Outline each Plasmodium falciparum-infected red blood cell.
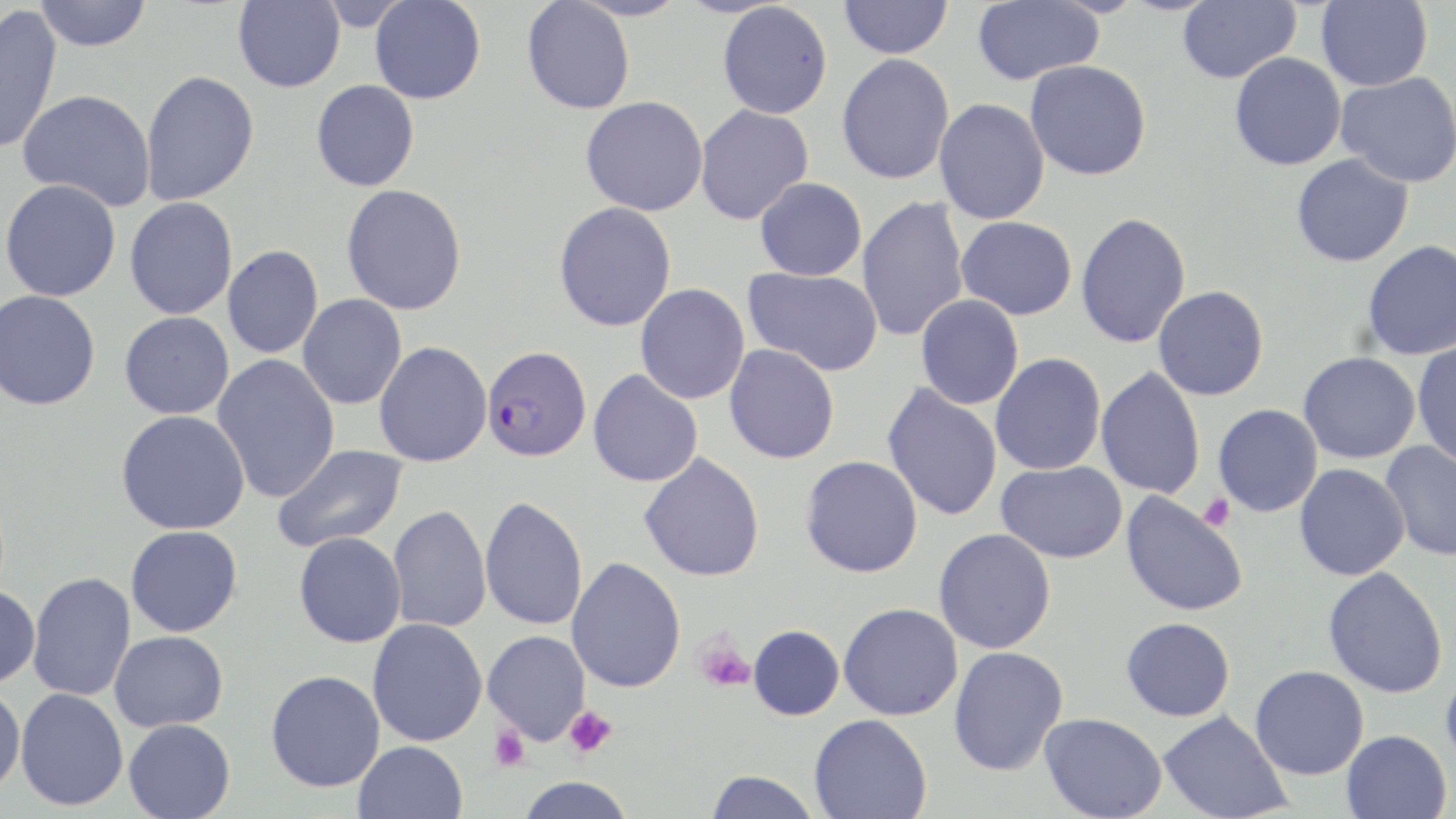
Approximate bounding boxes as (x1, y1, x2, y2) in pixels.
Plasmodium falciparum-infected red blood cells: (482, 345, 592, 462).

slide_level_diagnosis: Plasmodium falciparum
uninfected_red_blood_cell_locations: 'approximate bounding boxes as (x1, y1, x2, y2) in pixels: (34, 0, 152, 52), (233, 0, 345, 93), (370, 0, 485, 104), (838, 0, 953, 59), (971, 0, 1105, 85), (1177, 0, 1300, 83), (1316, 0, 1432, 91), (521, 1, 635, 114), (717, 2, 833, 119), (0, 3, 63, 156), (1229, 52, 1346, 170), (837, 53, 955, 185), (1025, 60, 1151, 181), (140, 70, 260, 206), (1336, 72, 1456, 188), (311, 80, 420, 192), (18, 89, 156, 212), (580, 96, 708, 216), (934, 98, 1050, 225), (695, 104, 814, 225), (1291, 153, 1414, 267), (755, 177, 867, 281), (1, 179, 121, 302), (341, 184, 467, 315), (125, 196, 238, 319), (856, 196, 969, 342), (553, 202, 677, 332), (1075, 212, 1191, 348), (956, 216, 1077, 320), (1362, 240, 1456, 360), (222, 245, 323, 359), (744, 267, 883, 376), (635, 284, 750, 404), (1153, 286, 1269, 400), (0, 290, 101, 410), (298, 294, 407, 410), (916, 295, 1024, 410), (119, 312, 234, 419), (374, 341, 492, 467), (1413, 342, 1456, 467), (724, 344, 840, 464), (1298, 352, 1420, 463), (990, 353, 1106, 475), (213, 354, 340, 504), (1095, 367, 1206, 500), (588, 369, 703, 487), (882, 384, 1003, 521), (1213, 404, 1323, 517), (116, 410, 250, 535), (1380, 441, 1456, 562), (272, 443, 408, 553), (639, 452, 765, 582), (801, 455, 923, 577), (996, 460, 1128, 563), (1294, 464, 1409, 581), (1121, 491, 1248, 617), (479, 495, 587, 631), (388, 505, 491, 633), (126, 525, 243, 637), (934, 529, 1056, 654), (294, 531, 406, 647), (567, 557, 687, 693), (1322, 566, 1449, 699), (28, 571, 136, 701), (0, 584, 40, 689), (839, 602, 963, 720), (1121, 617, 1235, 721), (367, 619, 487, 746), (748, 624, 844, 720), (110, 631, 228, 731), (483, 631, 590, 744), (948, 646, 1068, 776), (1440, 663, 1456, 771), (1250, 665, 1369, 780), (266, 670, 385, 792), (0, 686, 25, 796), (15, 687, 128, 811), (1158, 710, 1292, 819), (1039, 713, 1167, 819), (809, 714, 932, 819), (124, 718, 236, 819), (1341, 729, 1451, 819), (353, 741, 467, 819), (705, 770, 821, 819), (516, 777, 636, 819)'
platelet_locations: 'approximate bounding boxes as (x1, y1, x2, y2) in pixels: (1198, 493, 1236, 531), (695, 637, 755, 694), (563, 706, 617, 757), (490, 724, 531, 771)'
field_of_view: single
modality: light microscopy
preparation: thin blood smear
image_size: 1456×819 pixels
magnification: 1000x
stain: May-Grünwald-Giemsa